Report the malaria status of this cell.
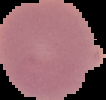

It is uninfected.

Segmented cell region on a black background. From a thin blood film. Image is 106×100 pixels.